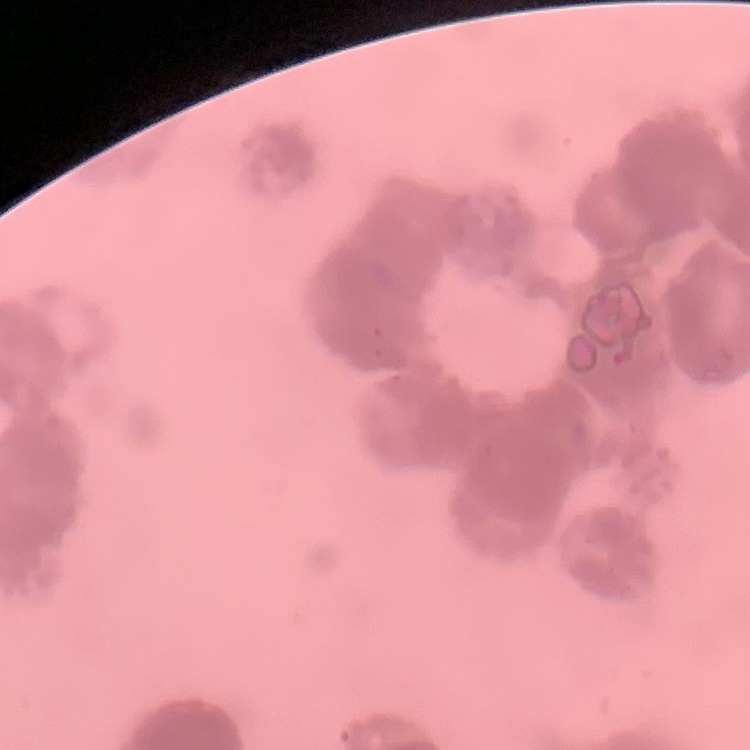
{
  "erythrocyte_morphology": "rouleaux formation",
  "image_type": "square crop of a larger photomicrograph",
  "preparation": "thin blood film",
  "stain": "Field's or Giemsa"
}